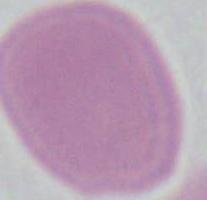

Summary:
  - Modality: micrograph
  - Magnification: 1000x
  - Identification: red blood cell